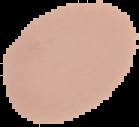 Image is 139×127 pixels. Cell region segmented out of the field of view; the surrounding area is masked to black. Result: no malaria parasites seen. From a thin blood smear.